Classify this cell by malaria status.
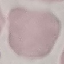

Uninfected.

preparation = thin blood film
stain = Giemsa
capture = smartphone camera at the microscope eyepiece
image type = automatically extracted cell patch, resized to 64 × 64 pixels